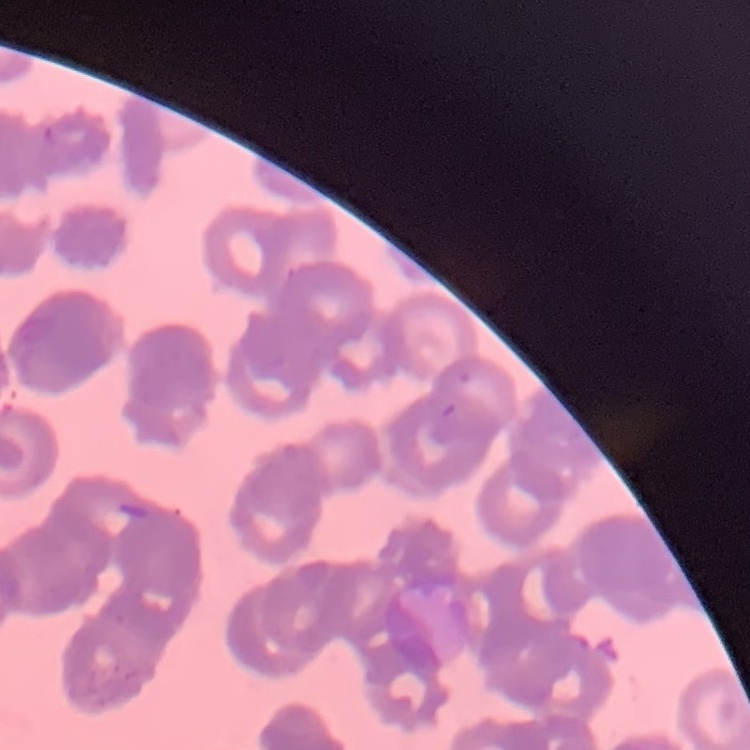

The red blood cells exhibit rouleaux formation. Square crop of a larger photomicrograph. Field's or Giemsa stain. Thin blood smear.